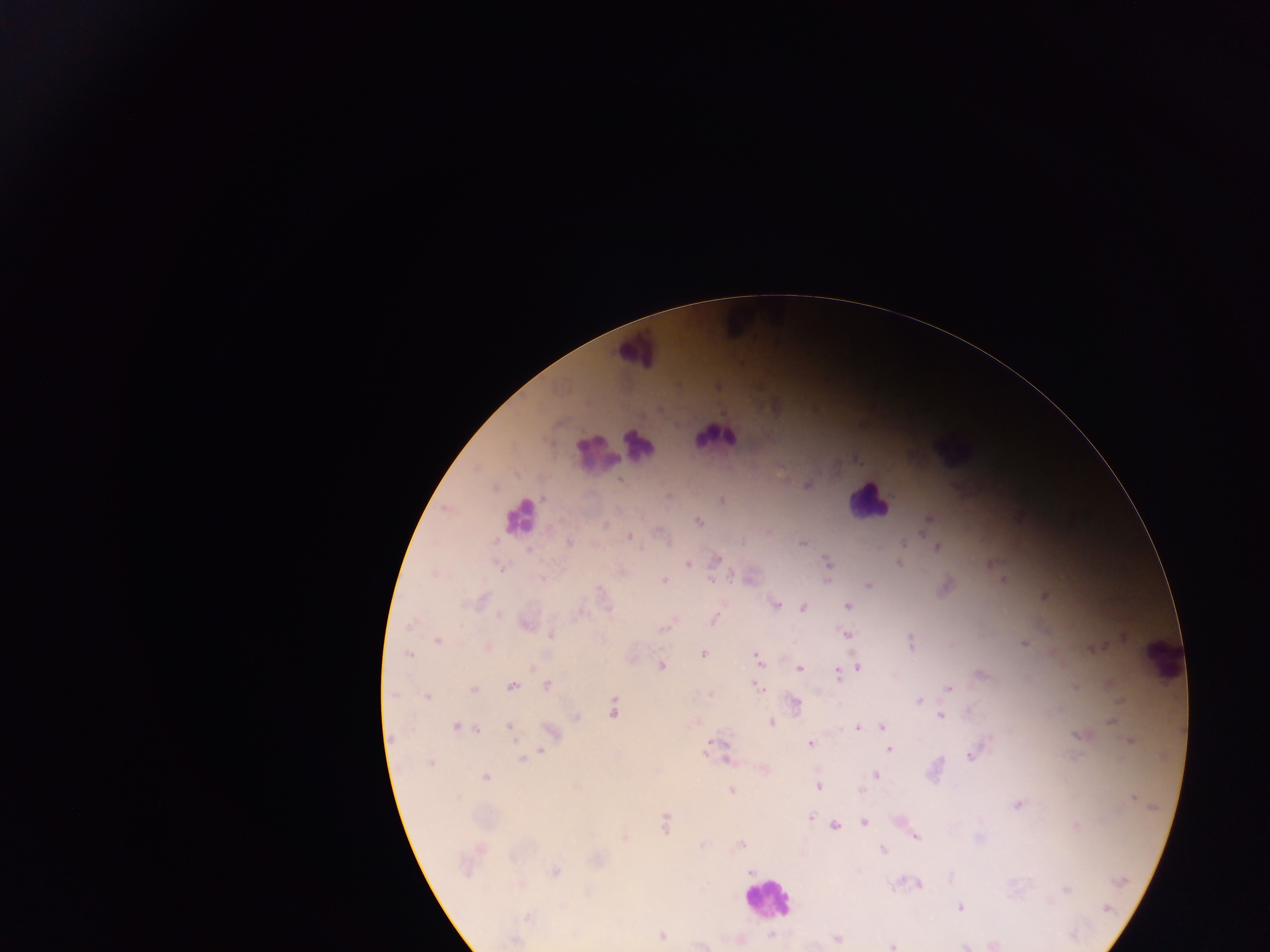

capture = mobile-phone photograph through a microscope
preparation = thick blood smear
image size = 1270×952 pixels
Plasmodium parasite locations = approximate centers as x y in pixels: 619 480; 808 485; 721 500; 698 522; 606 526; 922 533; 629 537; 570 543; 803 543; 904 543; 938 547; 716 559; 827 562; 688 564; 898 564; 501 567; 622 571; 541 579; 664 580; 711 580; 1003 580; 828 582; 867 585; 1045 595; 481 600; 777 605; 847 606; 803 608; 499 616; 713 622; 410 624; 526 624; 664 628; 551 635; 847 635; 438 640; 910 641; 1023 643; 1099 647; 488 648; 703 653; 408 654; 757 658; 661 666; 857 667; 799 668; 980 674; 837 675; 756 685; 513 686; 546 686; 1076 686; 948 688; 474 689; 392 694; 711 694; 427 697; 919 700; 796 702; 613 709; 940 716; 576 718; 1110 722; 771 723; 455 727; 882 727; 509 728; 857 728; 478 730; 551 731; 1078 736; 1129 741; 717 742; 810 743; 709 744; 889 749; 540 752; 970 756; 523 758; 430 763; 876 775; 486 777; 818 787; 731 790; 1133 799; 1018 804; 811 818; 864 822; 665 823; 835 825; 1076 826; 915 837; 625 838; 741 845; 883 849; 598 859; 554 872; 750 872; 1120 881; 919 884; 1066 889; 959 907; 1108 908; 527 917; 772 935; 662 936; 838 938; 514 940; 893 946
country = Ghana
field of view = single
leukocyte locations = approximate centers as x y in pixels: 739 316; 638 347; 715 437; 640 444; 948 446; 597 454; 865 502; 520 517; 1161 659; 767 900